Outline each P. falciparum parasite and classify it by life-cycle stage.
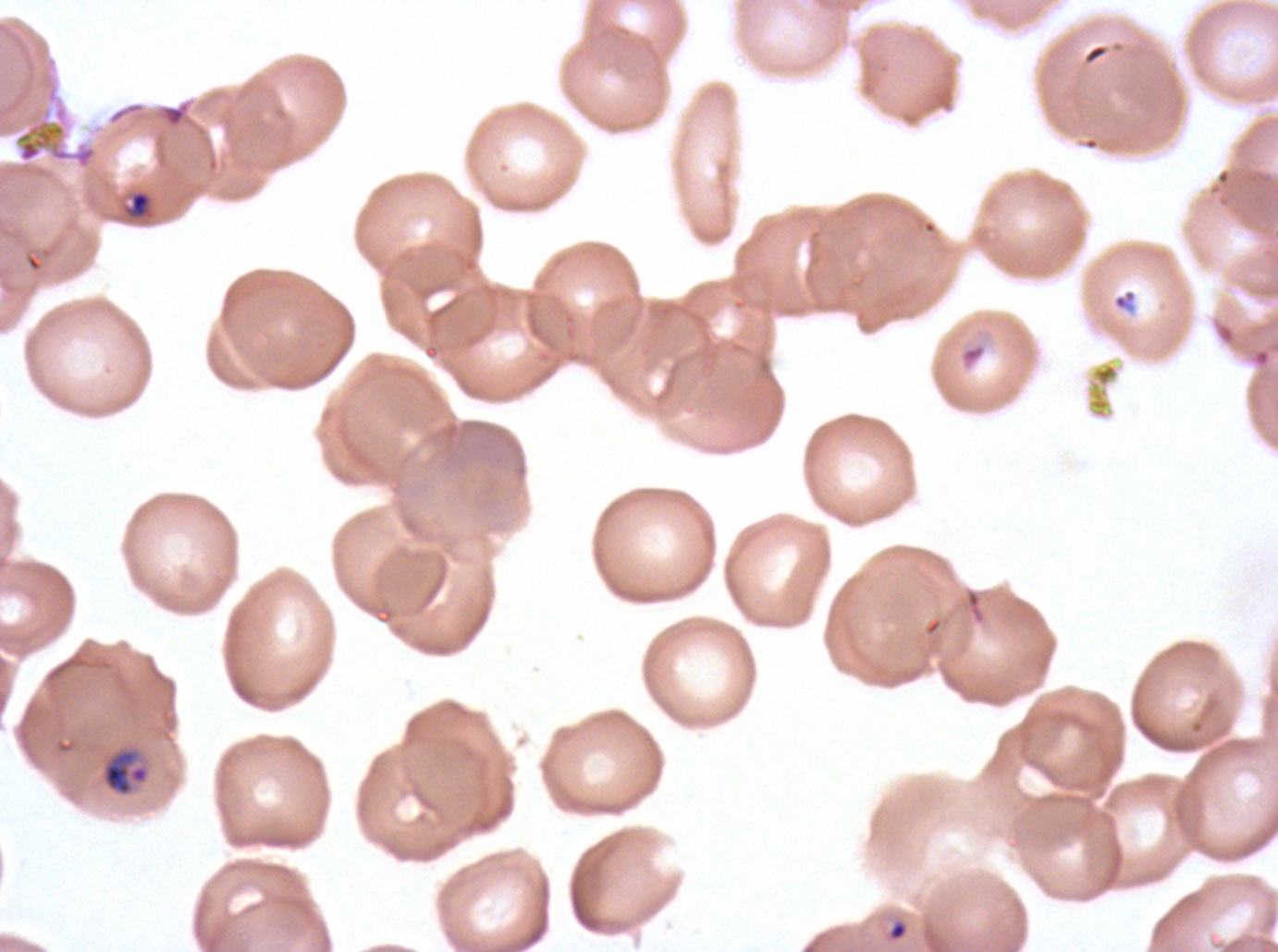
Approximate bounding boxes as [x1, y1, x2, y2] in pixels.
Rings: [1112, 287, 1137, 315], [889, 921, 907, 940].
Late-ring/early-trophozoite forms: [130, 191, 150, 215], [959, 342, 987, 370].
Mid trophozoites: [101, 747, 150, 797].
No late trophozoites, early schizonts, late schizonts, segmenters, or gametocytes observed.

Debris locations: [15, 118, 97, 169], [1247, 340, 1277, 370]. Giemsa stain. One sub-image of a larger composite. Life-cycle stages observed: ring, late-ring/early-trophozoite, mid trophozoite. Thin blood film. Image is 1278×952 pixels. Ex-vivo P. falciparum culture from a patient in The Gambia, grown for 24 to 48 hours.